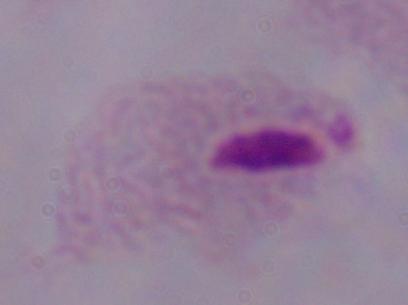
Summary:
  - Identification: trichomonad
  - Magnification: 1000x
  - Modality: micrograph